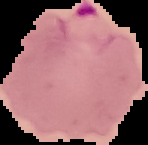

The area outside the segmented cell region is set to black. From a thin blood smear. Image is 148×145 pixels. Malaria status: parasitized.